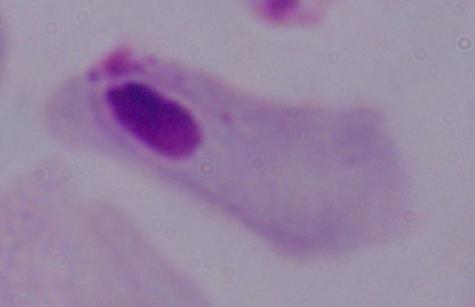 Captured at 1000x magnification. Photomicrograph. A trichomonad is seen.